Name the blood parasite species.
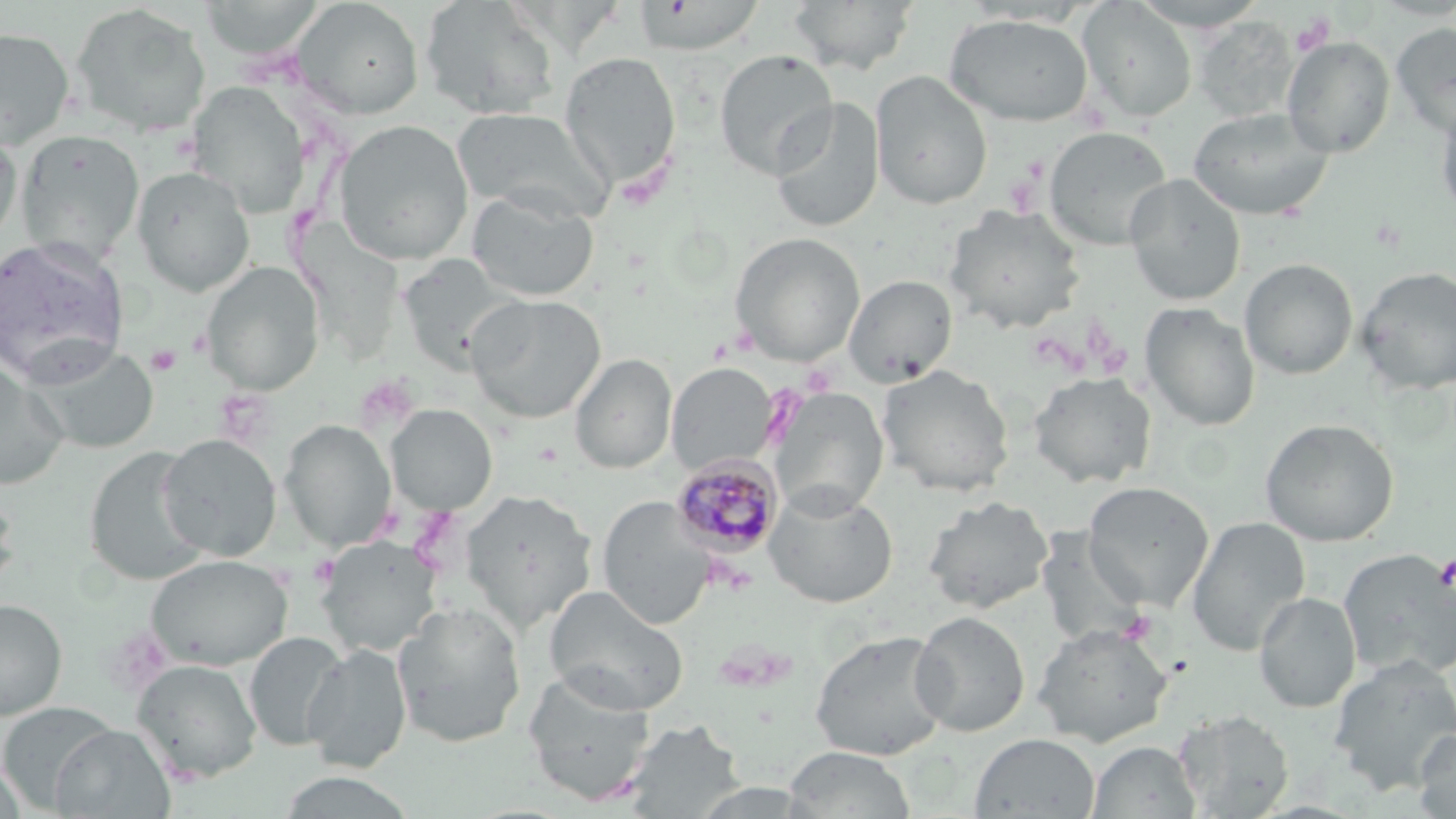
Plasmodium malariae.

Summary:
  - Coordinate format: approximate bounding boxes as [x1, y1, x2, y2] in pixels
  - Platelet locations: [1290, 13, 1333, 57], [1003, 168, 1042, 216], [1090, 333, 1130, 377], [146, 345, 182, 375], [308, 553, 341, 587], [1435, 555, 1456, 592], [1117, 610, 1156, 645]
  - Uninfected red blood cell locations: [197, 0, 328, 60], [293, 0, 424, 119], [419, 0, 560, 121], [1130, 0, 1271, 32], [633, 1, 766, 54], [786, 1, 920, 75], [1077, 1, 1197, 123], [70, 4, 211, 138], [943, 13, 1095, 127], [1193, 17, 1298, 122], [1390, 21, 1456, 139], [0, 27, 75, 149], [1282, 36, 1395, 158], [714, 49, 838, 181], [560, 51, 682, 192], [870, 70, 993, 210], [187, 81, 309, 215], [1435, 95, 1456, 223], [769, 97, 885, 234], [1187, 106, 1335, 221], [451, 107, 611, 222], [333, 119, 474, 265], [1043, 126, 1173, 250], [16, 128, 145, 265], [1, 129, 23, 247], [131, 166, 256, 297], [1124, 174, 1246, 306], [466, 188, 599, 301], [943, 203, 1087, 334], [729, 231, 866, 365], [0, 238, 133, 387], [396, 255, 519, 373], [1239, 258, 1358, 379], [202, 261, 324, 395], [1355, 265, 1456, 395], [843, 274, 958, 387], [465, 294, 606, 423], [1140, 302, 1261, 431], [33, 344, 158, 454], [570, 353, 677, 474], [0, 361, 70, 489], [666, 362, 778, 474], [877, 364, 1015, 497], [1029, 372, 1157, 488], [770, 387, 889, 516], [386, 404, 497, 515], [1259, 417, 1400, 546], [279, 419, 396, 551], [157, 433, 281, 561], [83, 446, 210, 586], [1082, 481, 1215, 610], [0, 483, 21, 597], [764, 485, 898, 608], [461, 489, 597, 634], [922, 495, 1054, 614], [597, 496, 715, 630], [1187, 516, 1310, 656], [1034, 529, 1148, 648], [317, 537, 443, 656], [1338, 549, 1456, 680], [146, 554, 293, 671], [543, 586, 689, 715], [1254, 592, 1360, 713], [0, 599, 67, 720], [391, 601, 527, 747], [910, 610, 1031, 737], [1033, 624, 1173, 746], [809, 629, 952, 760], [244, 631, 347, 751], [303, 643, 412, 773], [1328, 655, 1456, 796], [132, 659, 262, 784], [521, 669, 658, 808], [0, 701, 118, 812], [1173, 709, 1294, 818], [622, 719, 744, 817], [50, 724, 174, 818], [1414, 727, 1456, 819], [970, 733, 1100, 819], [1088, 741, 1202, 819], [782, 746, 917, 819], [0, 762, 27, 819]
  - Plasmodium malariae-infected red blood cell locations: [670, 454, 784, 559]
  - Modality: optical microscopy
  - Preparation: thin blood smear
  - Stain: May-Grünwald-Giemsa
  - Image size: 1456×819 pixels
  - Field of view: single
  - Magnification: 1000x